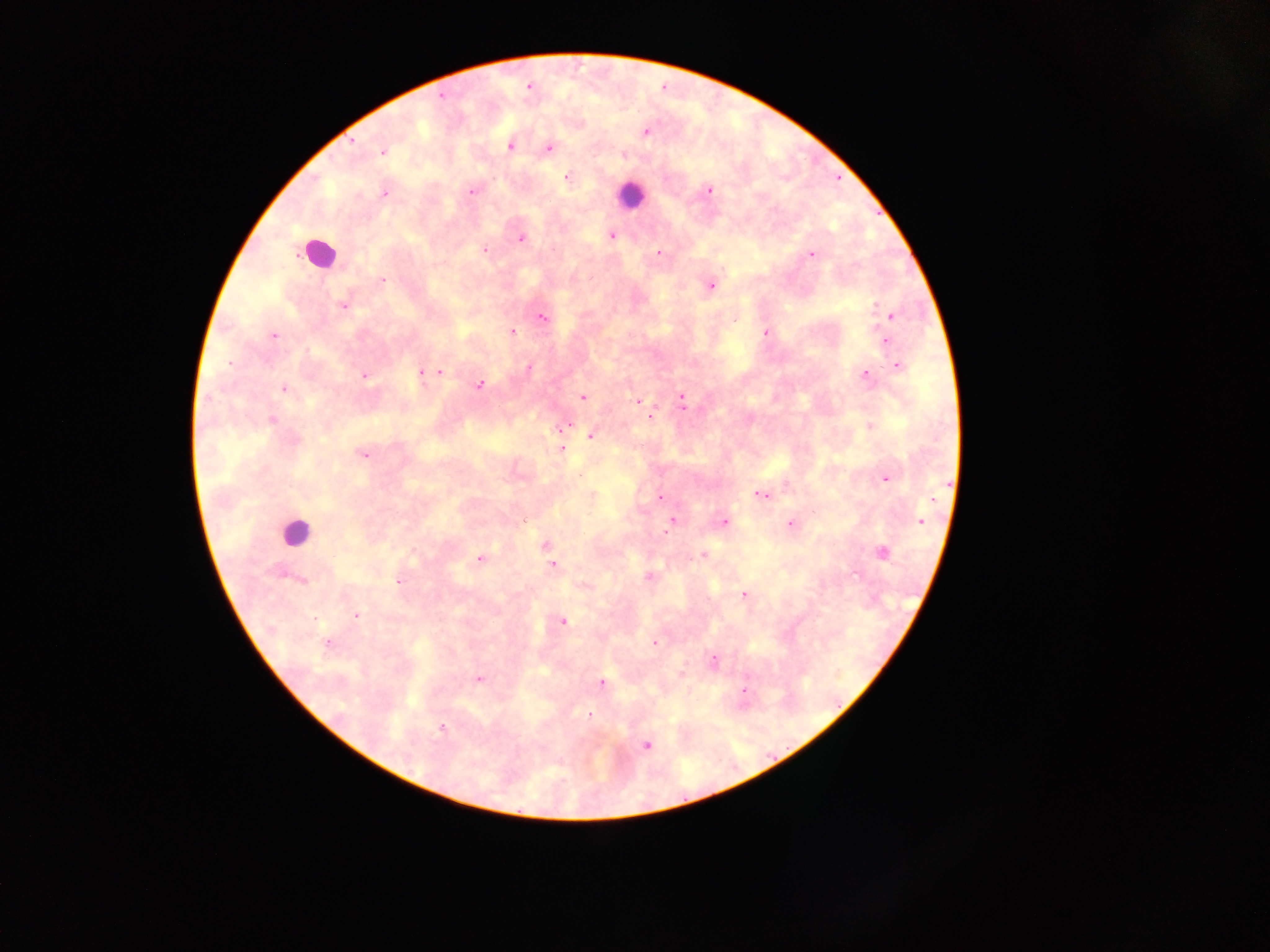

image_size: 1270×952 pixels
preparation: thick blood film
capture: mobile-phone photograph through a microscope
leukocyte_locations: 'approximate centers as x y in pixels: 630 194; 318 252; 296 531'
field_of_view: single
plasmodium_parasite_locations: 'approximate centers as x y in pixels: 528 87; 440 95; 645 131; 510 146; 548 147; 382 151; 622 154; 567 177; 709 190; 471 191; 384 194; 611 235; 520 238; 484 249; 658 252; 811 254; 382 280; 710 285; 343 304; 892 315; 541 317; 512 332; 766 332; 274 335; 885 341; 896 365; 527 369; 440 371; 422 373; 865 374; 364 375; 480 384; 283 388; 583 397; 681 397; 638 400; 648 416; 271 420; 870 425; 562 427; 591 434; 561 450; 362 454; 579 475; 885 478; 760 495; 660 497; 672 520; 920 521; 723 522; 791 524; 545 544; 881 552; 702 554; 480 558; 552 565; 649 577; 302 580; 398 581; 584 585; 744 595; 355 615; 561 620; 653 643; 327 644; 713 660; 681 674; 478 678; 601 683; 743 691; 589 716; 442 729; 646 744'
country: Ghana